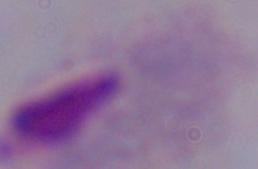

1000x magnification. Photomicrograph. A trichomonad is shown.